Give the preparation type.
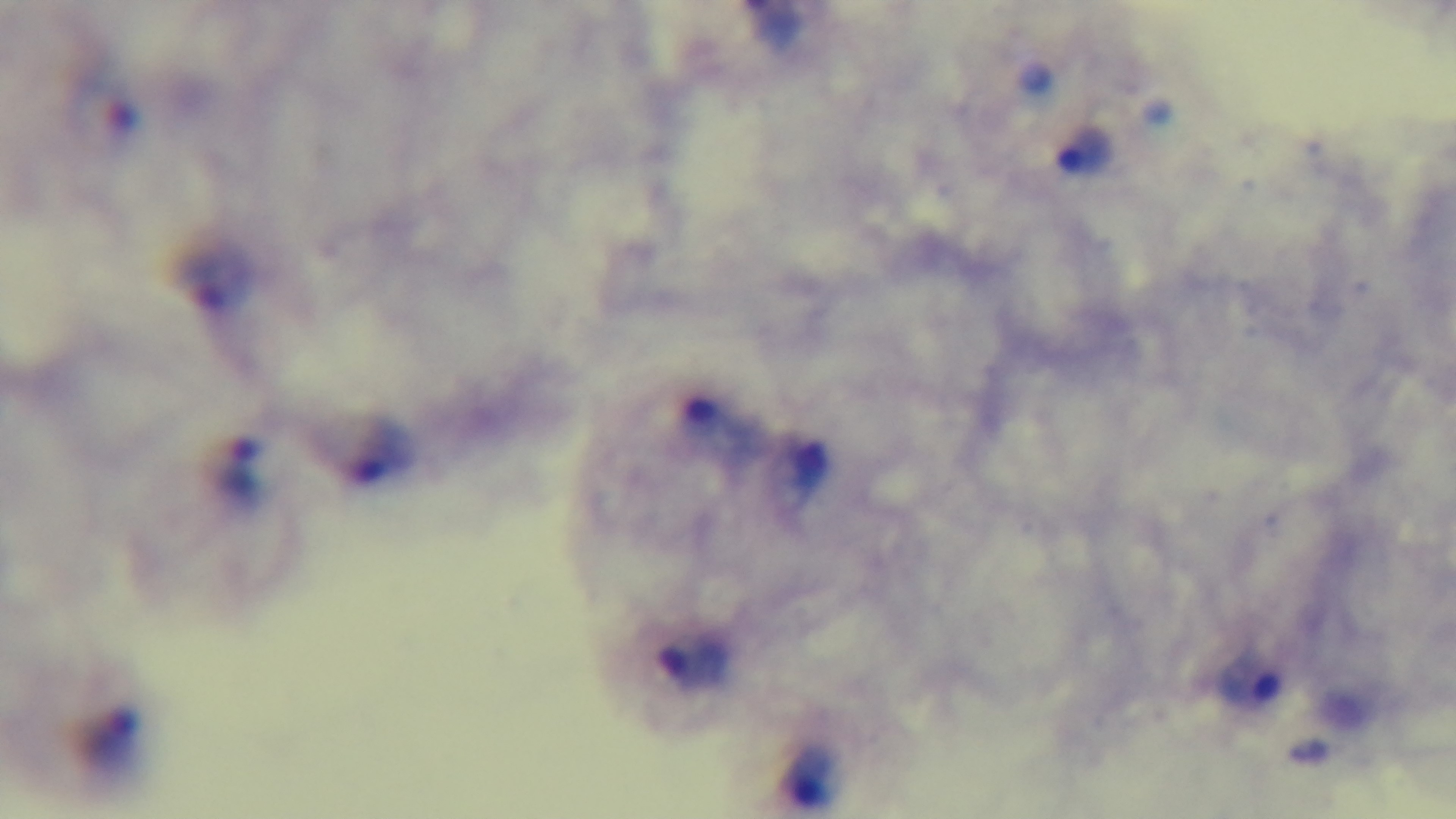

A thick smear.

Summary:
  - Modality: light microscopy
  - Objective: 100x oil immersion
  - Stain: Giemsa
  - Field of view: one from the slide
  - Capture: mounted 4K digital camera
  - Malaria status: infected